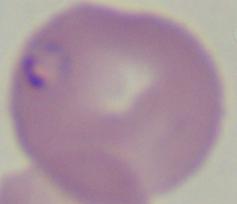

Summary:
  - Modality: micrograph
  - Identification: Babesia
  - Magnification: 1000x